Classify this cell by malaria status.
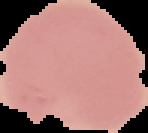
It is uninfected.

Image is 148×133 pixels. From a thin blood film. The area outside the segmented cell region is set to black.